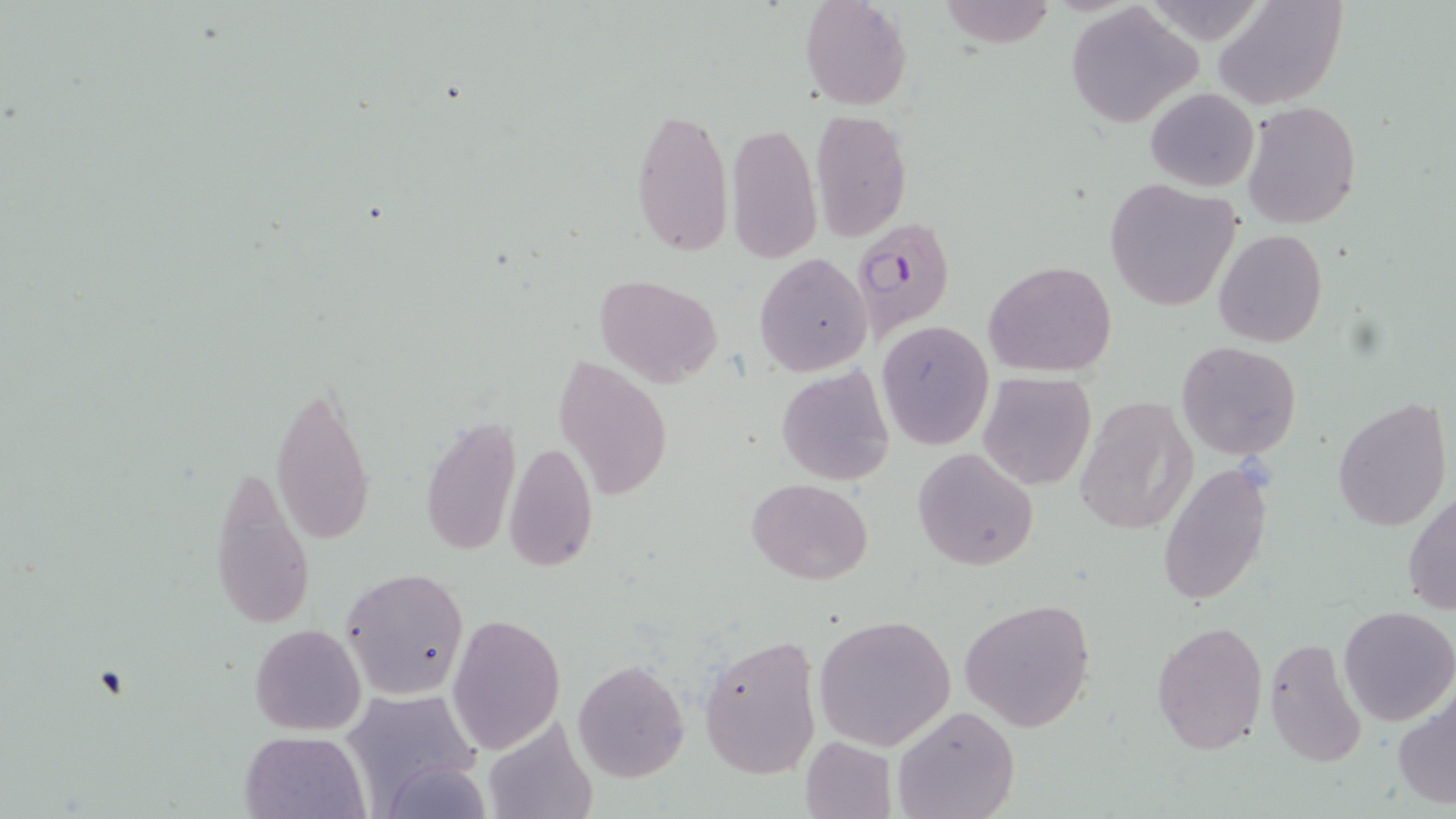 Approximate bounding boxes as (x1,y1)-(x2,y2) corner pairs in pixels. Uninfected red blood cell locations: (799,0)-(913,110), (939,0)-(1056,48), (1212,0)-(1348,111), (1065,4)-(1203,129), (1145,87)-(1259,191), (1244,101)-(1361,228), (630,105)-(733,257), (810,107)-(912,242), (726,120)-(820,265), (1104,179)-(1240,312), (1214,229)-(1326,347), (753,253)-(872,375), (983,260)-(1117,378), (596,275)-(722,387), (876,322)-(993,448), (1177,341)-(1301,461), (551,356)-(673,502), (776,367)-(894,487), (977,372)-(1096,491), (268,380)-(377,547), (1076,396)-(1197,534), (1333,397)-(1452,534), (421,418)-(520,558), (504,443)-(599,571), (912,447)-(1039,570), (210,459)-(316,631), (1157,462)-(1273,607), (746,478)-(873,584), (1404,492)-(1456,617), (342,568)-(468,700), (958,599)-(1095,734), (1339,606)-(1456,726), (444,613)-(566,755), (814,614)-(955,750), (1152,620)-(1268,754), (249,622)-(366,735), (697,635)-(821,780), (1263,635)-(1371,770), (572,659)-(689,783), (338,687)-(483,812), (1393,689)-(1456,813), (892,705)-(1019,819), (241,730)-(368,818), (800,735)-(897,819). Plasmodium falciparum-infected red blood cell locations: (850,218)-(955,338). Slide-level diagnosis: Plasmodium falciparum. May-Grünwald-Giemsa stain. One field of a larger specimen. 1000x magnification. Thin blood smear. Image is 1456×819 pixels. Optical microscopy.